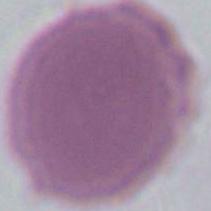

Summary:
  - Identification: red blood cell
  - Modality: micrograph
  - Magnification: 1000x